Locate and identify every blood parasite.
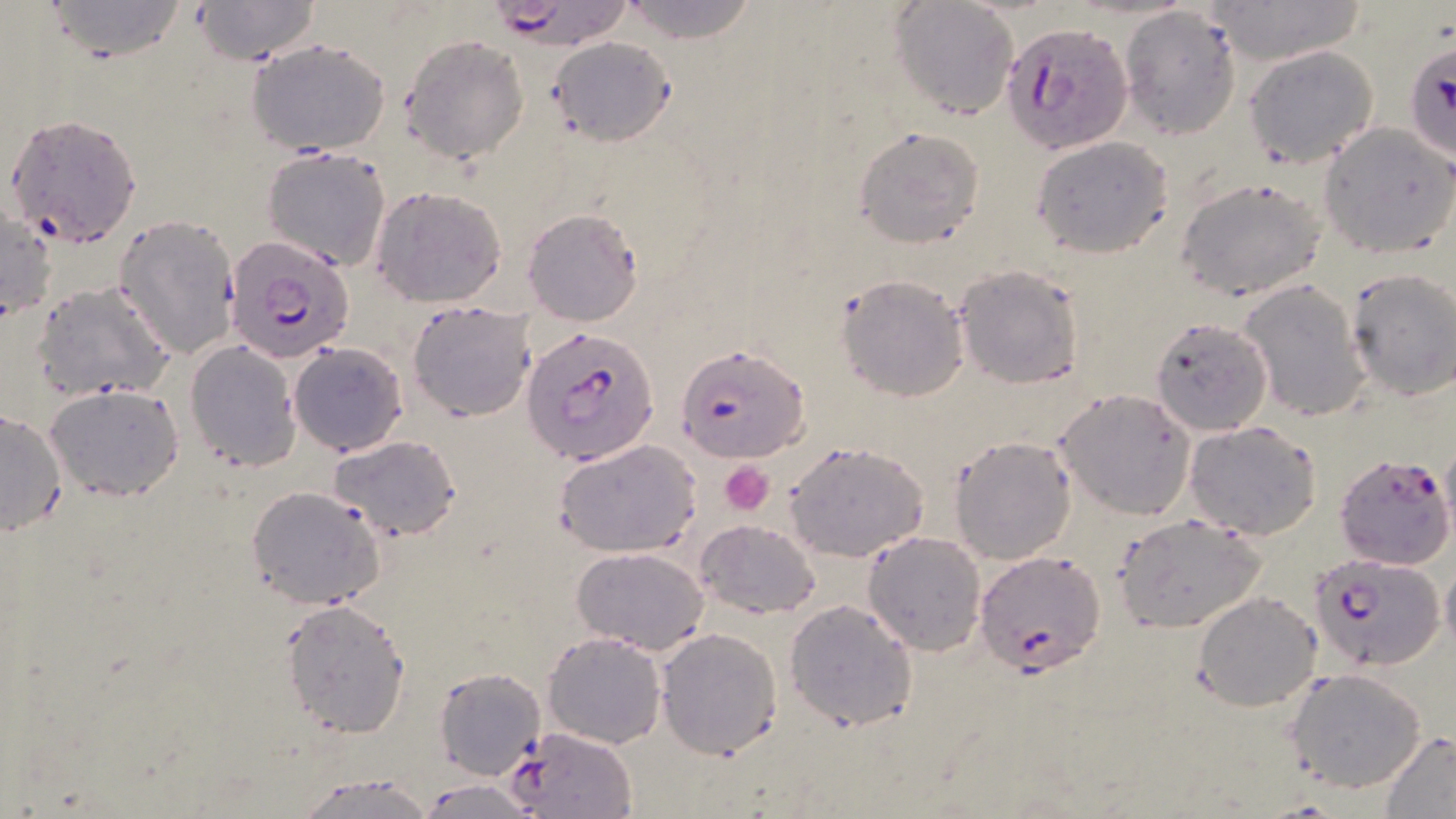

Approximate bounding boxes as (x1,y1)-(x2,y2) corner pairs in pixels.
Plasmodium falciparum-infected red blood cells: (477,0)-(637,51), (1003,21)-(1132,153), (1403,39)-(1456,165), (5,113)-(145,249), (224,231)-(356,365), (522,326)-(660,466), (676,344)-(808,462), (1334,453)-(1453,569), (976,550)-(1104,674), (1307,553)-(1443,674).
No Plasmodium ovale, Plasmodium malariae, Plasmodium vivax, Babesia divergens, or Trypanosoma brucei observed.

Platelet locations: (720,461)-(773,515). Uninfected red blood cell locations: (44,0)-(188,61), (189,0)-(320,64), (619,0)-(759,43), (889,0)-(1019,120), (1211,0)-(1359,67), (1117,5)-(1244,139), (401,35)-(530,163), (548,36)-(676,147), (246,37)-(390,157), (1244,44)-(1381,170), (1320,123)-(1455,257), (855,126)-(985,248), (1031,136)-(1174,258), (261,147)-(391,270), (1175,176)-(1328,301), (372,186)-(508,307), (1,203)-(56,321), (522,207)-(645,326), (114,214)-(240,361), (954,265)-(1083,389), (1345,270)-(1456,400), (836,272)-(969,402), (1238,280)-(1371,421), (33,281)-(176,403), (407,299)-(536,423), (1151,317)-(1275,437), (185,340)-(302,471), (290,343)-(408,458), (45,383)-(185,501), (1055,389)-(1196,520), (0,406)-(68,535), (1183,420)-(1323,539), (328,434)-(463,541), (948,435)-(1076,565), (555,438)-(701,557), (784,440)-(929,563), (246,486)-(389,607), (1114,514)-(1265,633), (693,518)-(823,618), (862,530)-(987,655), (572,547)-(710,655), (1193,591)-(1321,711), (785,598)-(917,733), (280,599)-(412,737), (656,627)-(784,758), (543,631)-(668,748), (434,666)-(546,778), (1286,668)-(1429,793), (506,725)-(641,819), (1379,731)-(1456,817), (293,770)-(439,819), (416,777)-(546,818). Slide-level diagnosis: Plasmodium falciparum. Thin blood film. Single field of view. May-Grünwald-Giemsa-stained preparation. Captured at 1000x magnification. Optical microscopy. Image is 1456×819 pixels.